Point out every malaria parasite and every leukocyte.
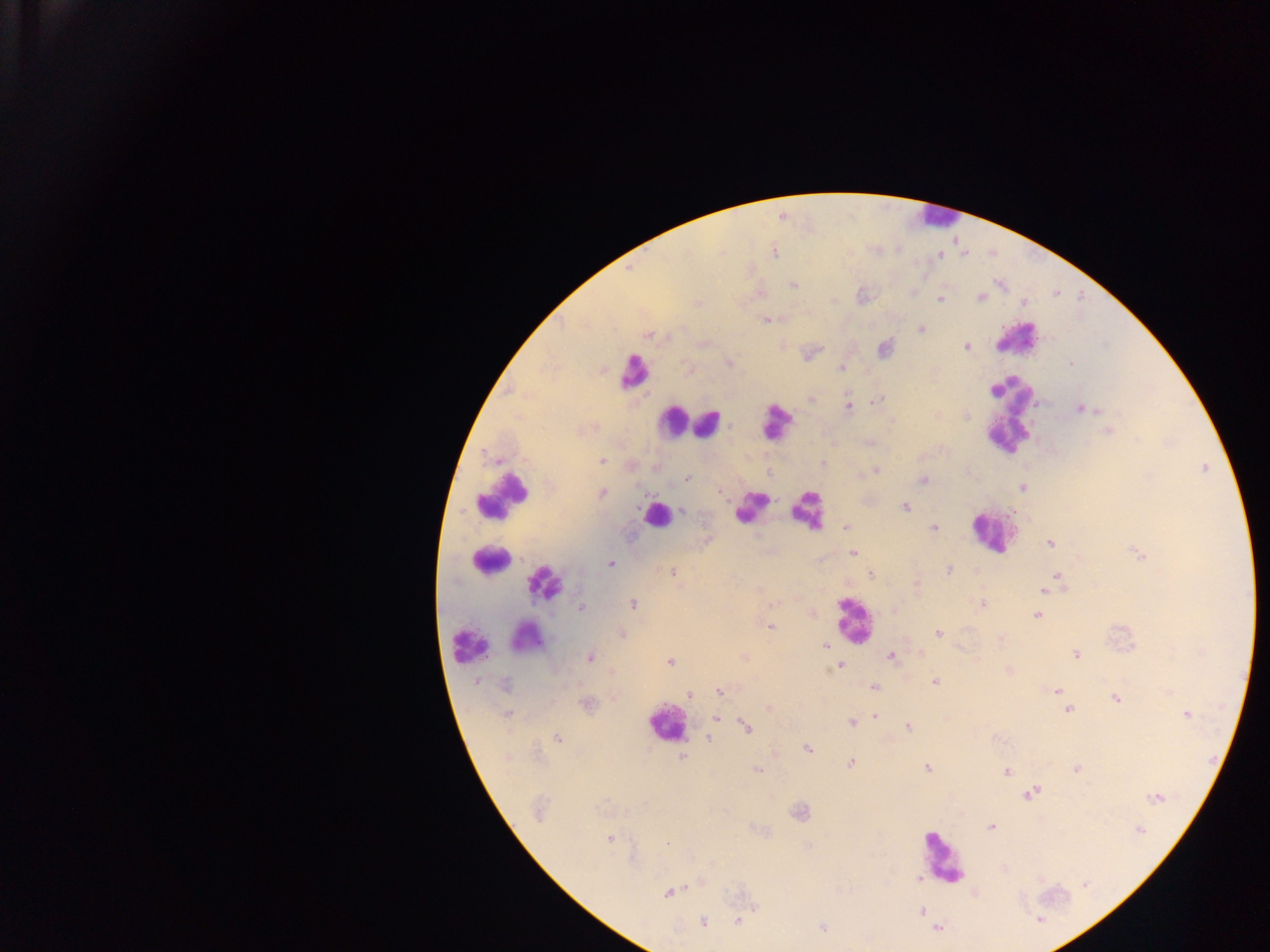

Approximate centers as [x, y] in pixels.
Malaria parasites: [774, 253], [940, 255], [793, 285], [980, 298], [939, 299], [697, 303], [1025, 303], [765, 320], [921, 329], [649, 335], [966, 347], [729, 363], [1071, 363], [841, 368], [812, 399], [878, 400], [848, 407], [1080, 409], [967, 415], [1108, 430], [603, 461], [823, 463], [876, 470], [687, 477], [923, 480], [1022, 487], [718, 491], [603, 494], [905, 507], [682, 511], [934, 527], [846, 528], [1050, 543], [853, 553], [610, 563], [948, 570], [671, 572], [870, 574], [1057, 575], [917, 584], [1044, 590], [633, 604], [983, 605], [581, 608], [1036, 616], [770, 626], [938, 633], [621, 635], [825, 646], [1076, 654], [890, 656], [590, 658], [670, 662], [840, 665], [935, 682], [505, 685], [874, 687], [1057, 690], [719, 691], [690, 695], [1116, 699], [1068, 711], [1187, 714], [507, 715], [876, 715], [717, 718], [851, 722], [746, 727], [908, 728], [556, 738], [709, 739], [808, 748], [682, 758], [850, 762], [927, 767], [1077, 769], [758, 770], [1006, 771], [1032, 792], [1156, 797], [537, 811], [800, 813], [991, 826], [1141, 830], [609, 839], [667, 843], [918, 877], [1085, 884], [668, 893], [755, 908], [922, 912], [1039, 920], [737, 921], [704, 922], [823, 928], [937, 928].
Leukocytes: [934, 216], [1016, 337], [633, 373], [1008, 415], [773, 421], [674, 422], [708, 423], [504, 495], [750, 506], [806, 510], [656, 515], [990, 531], [488, 560], [545, 583], [854, 620], [525, 637], [467, 643], [665, 724], [942, 859].

Image is 1270×952 pixels. One field of view. Mobile-phone photograph taken through the microscope. Thick blood film. Sample from Ghana.